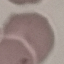 Malaria status: uninfected. Cell patch, automatically extracted from a larger field of view and resized to 64 × 64 pixels. Thin smear of blood. Photographed with a smartphone camera at the microscope eyepiece. Giemsa stain.